Assess this cell for malaria.
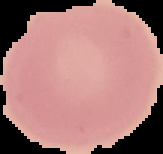
Uninfected.

Summary:
  - Image type: cell region segmented out of the field of view; surrounding area masked to black
  - Image size: 163×154 pixels
  - Preparation: thin blood film